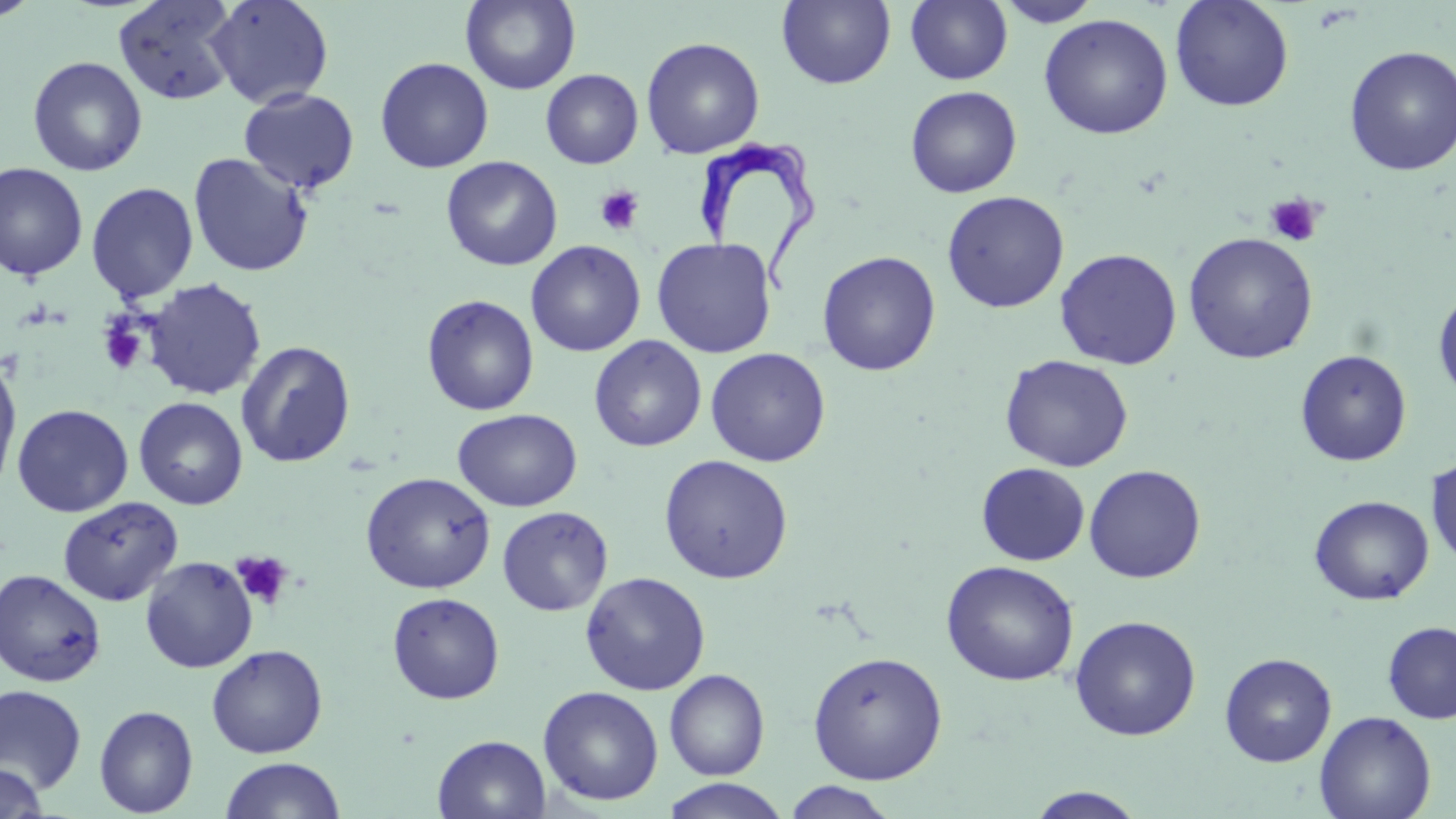
Approximate bounding boxes as (x1, y1, x2, y2) in pixels. Uninfected red blood cell locations: (0, 0, 42, 23), (113, 0, 240, 105), (205, 0, 334, 109), (461, 0, 580, 94), (777, 0, 895, 89), (906, 0, 1013, 85), (1170, 0, 1294, 113), (993, 1, 1104, 27), (1038, 13, 1173, 140), (641, 37, 765, 159), (1343, 45, 1456, 177), (27, 56, 147, 176), (375, 57, 494, 173), (541, 69, 643, 169), (905, 86, 1022, 198), (238, 87, 361, 194), (188, 152, 314, 277), (441, 156, 563, 271), (0, 162, 88, 281), (86, 181, 199, 303), (941, 190, 1070, 313), (1183, 232, 1318, 364), (651, 237, 777, 358), (526, 240, 646, 357), (1054, 248, 1182, 370), (817, 251, 941, 377), (143, 279, 267, 401), (1433, 289, 1456, 404), (422, 294, 539, 416), (589, 336, 706, 452), (236, 340, 356, 469), (705, 347, 831, 467), (1295, 350, 1412, 467), (1000, 354, 1134, 472), (0, 355, 22, 496), (133, 397, 248, 510), (12, 403, 133, 517), (453, 408, 582, 512), (659, 454, 794, 584), (1425, 456, 1456, 570), (976, 462, 1090, 565), (1084, 464, 1206, 583), (361, 471, 496, 594), (1309, 495, 1434, 605), (57, 496, 183, 606), (497, 506, 613, 616), (140, 556, 257, 673), (941, 559, 1079, 686), (0, 569, 107, 687), (580, 571, 711, 695), (387, 592, 505, 704), (1069, 615, 1201, 741), (1383, 621, 1456, 724), (206, 644, 328, 758), (807, 650, 947, 784), (1220, 653, 1337, 766), (664, 669, 770, 780), (0, 685, 87, 796), (538, 686, 664, 807), (94, 705, 199, 817), (1315, 710, 1436, 819), (432, 734, 551, 819), (219, 757, 346, 818), (0, 764, 48, 818), (660, 779, 791, 819), (781, 781, 900, 819), (1025, 787, 1147, 818). Platelet locations: (594, 184, 644, 235), (1263, 194, 1324, 247), (98, 318, 148, 375), (231, 550, 294, 610). Trypanosoma brucei locations: (691, 140, 819, 299). Slide-level diagnosis: Trypanosoma brucei. Thin blood film. May-Grünwald-Giemsa-stained preparation. 1000x magnification. One field of a larger specimen. Image is 1456×819 pixels. Light microscopy.